Locate every blood parasite and identify its species.
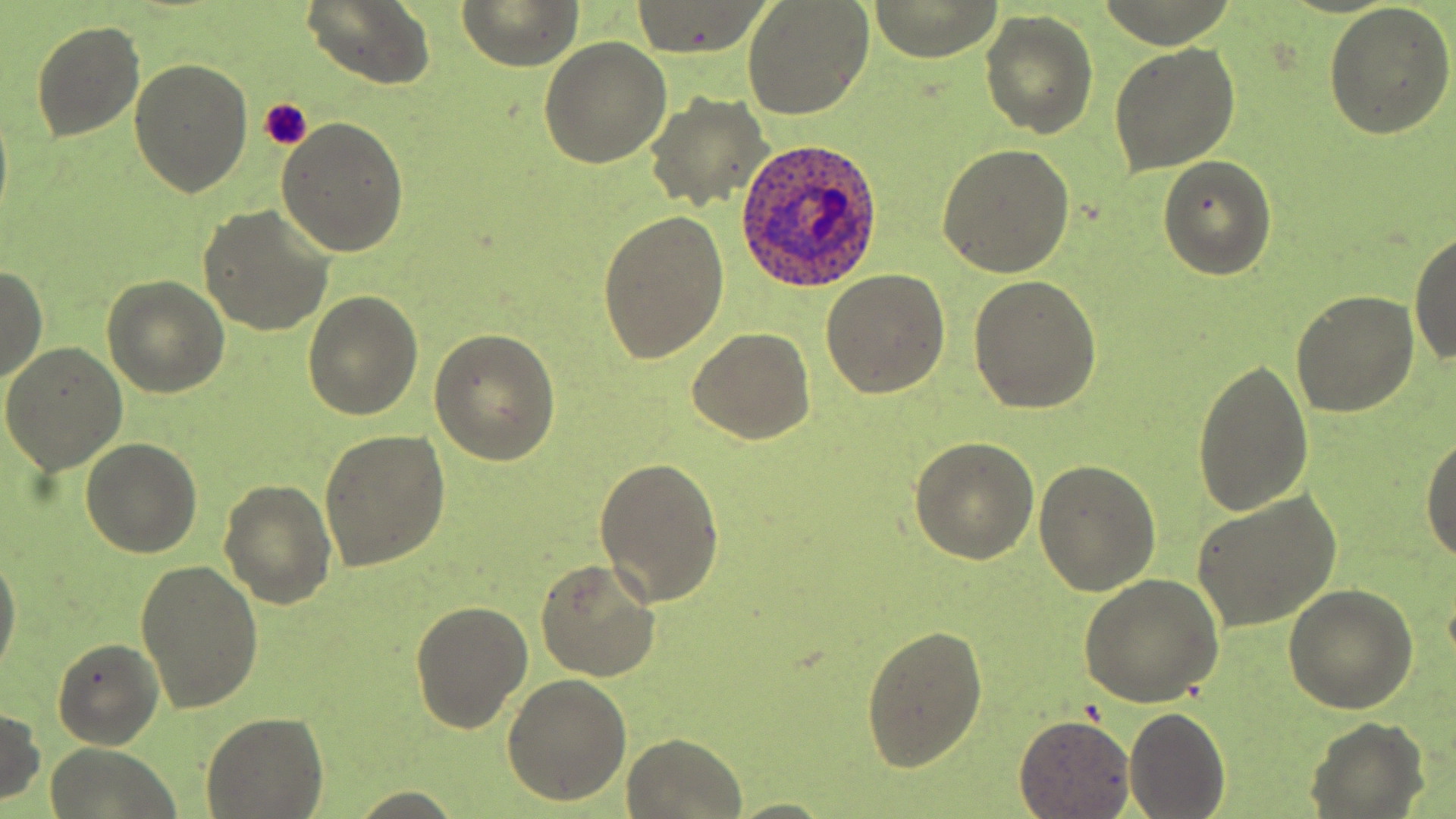

Approximate bounding boxes as (x1, y1, x2, y2) in pixels.
Plasmodium ovale-infected red blood cells: (735, 137, 884, 291).
No Plasmodium falciparum, Plasmodium malariae, Plasmodium vivax, Babesia divergens, or Trypanosoma brucei observed.

slide-level diagnosis = Plasmodium ovale
image size = 1456×819 pixels
platelet locations = approximate bounding boxes as (x1, y1, x2, y2) in pixels: (257, 98, 311, 149)
preparation = thin blood film
stain = May-Grünwald-Giemsa
modality = optical microscopy
uninfected red blood cell locations = approximate bounding boxes as (x1, y1, x2, y2) in pixels: (459, 0, 582, 70), (867, 0, 1004, 62), (301, 1, 436, 90), (741, 1, 876, 120), (629, 2, 773, 59), (1324, 3, 1456, 140), (980, 10, 1098, 138), (30, 19, 146, 142), (538, 38, 673, 170), (1109, 45, 1241, 175), (129, 58, 253, 198), (645, 91, 773, 214), (276, 116, 409, 258), (937, 144, 1076, 278), (1157, 155, 1276, 280), (198, 204, 336, 337), (599, 211, 730, 363), (1409, 227, 1456, 369), (0, 266, 47, 385), (821, 267, 951, 398), (969, 274, 1101, 414), (102, 276, 230, 397), (1291, 289, 1420, 416), (304, 291, 424, 420), (431, 328, 562, 465), (688, 329, 817, 444), (1, 341, 129, 475), (1192, 358, 1315, 518), (1419, 427, 1456, 568), (318, 429, 450, 572), (79, 436, 202, 557), (909, 438, 1040, 565), (596, 454, 724, 608), (1034, 459, 1160, 598), (219, 479, 337, 609), (1190, 491, 1341, 633), (0, 549, 21, 680), (536, 559, 661, 682), (136, 560, 263, 713), (1080, 574, 1225, 707), (1284, 585, 1418, 715), (410, 599, 534, 735), (862, 622, 988, 772), (51, 637, 165, 750), (503, 674, 632, 805), (1123, 704, 1229, 818), (0, 706, 45, 806), (202, 710, 328, 818), (1014, 715, 1136, 817), (1306, 718, 1427, 816), (621, 734, 748, 819), (45, 743, 182, 818), (343, 789, 468, 819), (724, 797, 838, 818)
field of view = single
magnification = 1000x